Identify the parasite.
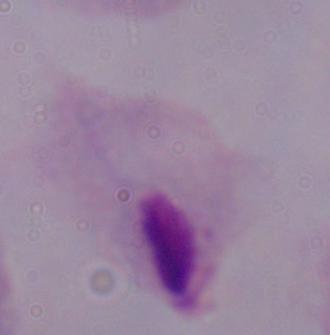

This is a trichomonad.

Summary:
  - Magnification: 1000x
  - Modality: photomicrograph